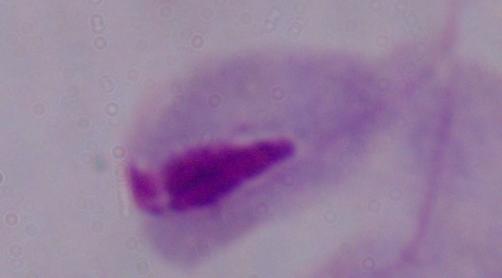
Summary:
  - Identification: trichomonad
  - Modality: photomicrograph
  - Magnification: 1000x